Describe the morphology of the erythrocytes.
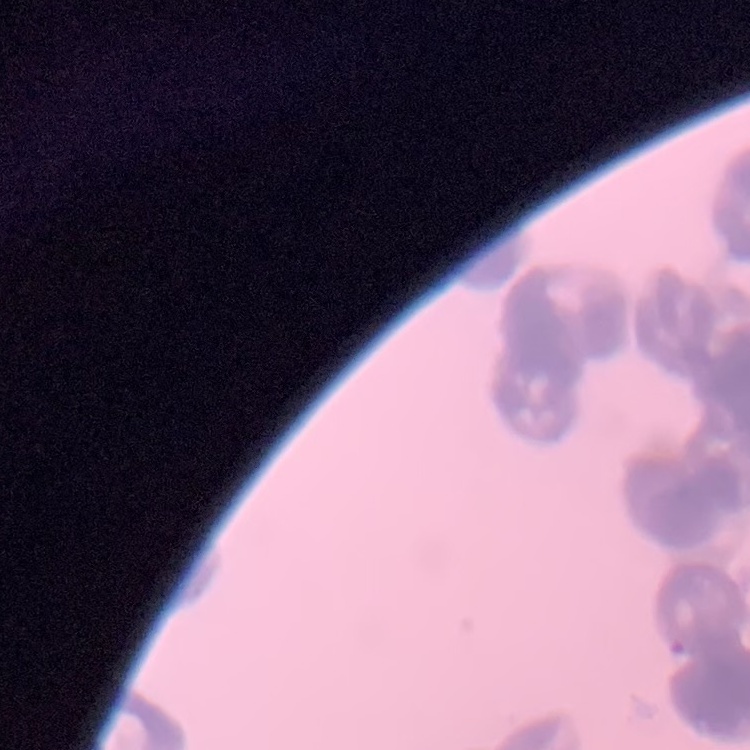

They show rouleaux formation.

stain = Field's or Giemsa
image type = one tile cut from a larger photomicrograph
preparation = thin blood film